Locate every malaria parasite.
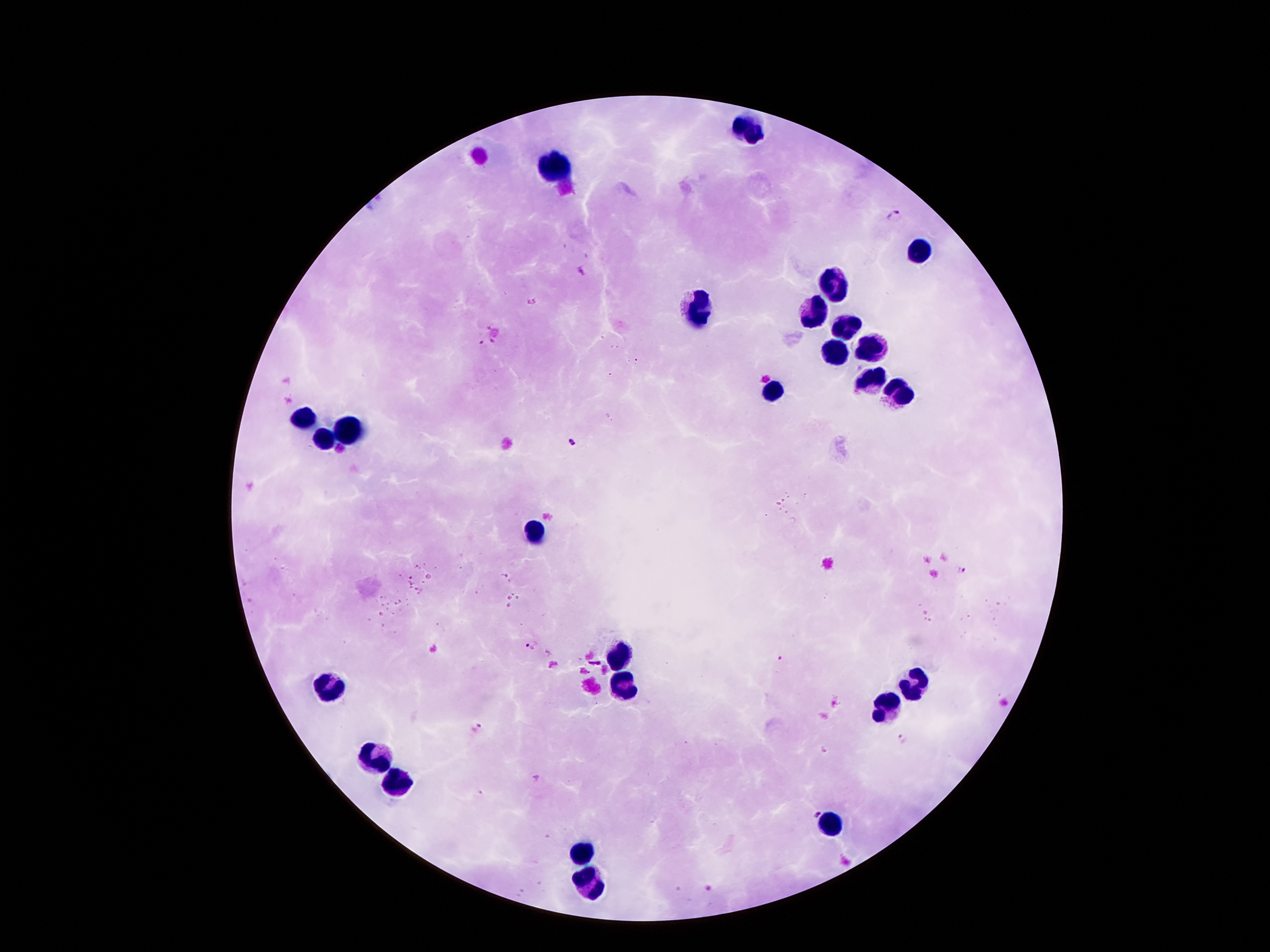

Approximate centers as [x, y] in pixels.
Malaria parasites: [893, 215], [479, 343], [571, 443], [961, 571], [532, 645], [782, 659], [476, 727], [902, 738], [813, 812], [709, 888].

leukocyte locations = [744, 129], [555, 166], [921, 250], [837, 286], [699, 309], [814, 314], [844, 330], [867, 348], [835, 354], [873, 380], [774, 391], [892, 391], [304, 422], [345, 432], [324, 443], [535, 532], [619, 661], [916, 682], [335, 684], [622, 688], [887, 707], [374, 761], [392, 786], [830, 829], [583, 852], [590, 884]
stain = Giemsa
patient malaria status = positive for Plasmodium falciparum
preparation = thick peripheral-blood smear
image size = 1270×952 pixels
field of view = one from this slide
capture = smartphone through the microscope eyepiece
magnification = 100x